Assess the morphology of the red blood cells.
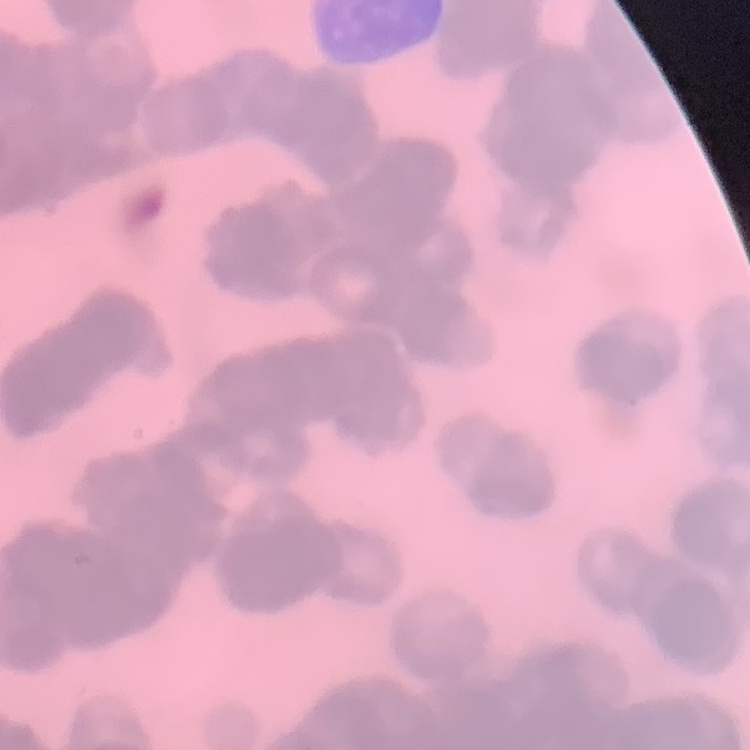

Rouleaux formation.

image type = square crop of a larger photomicrograph
preparation = thin blood film
stain = Field's or Giemsa